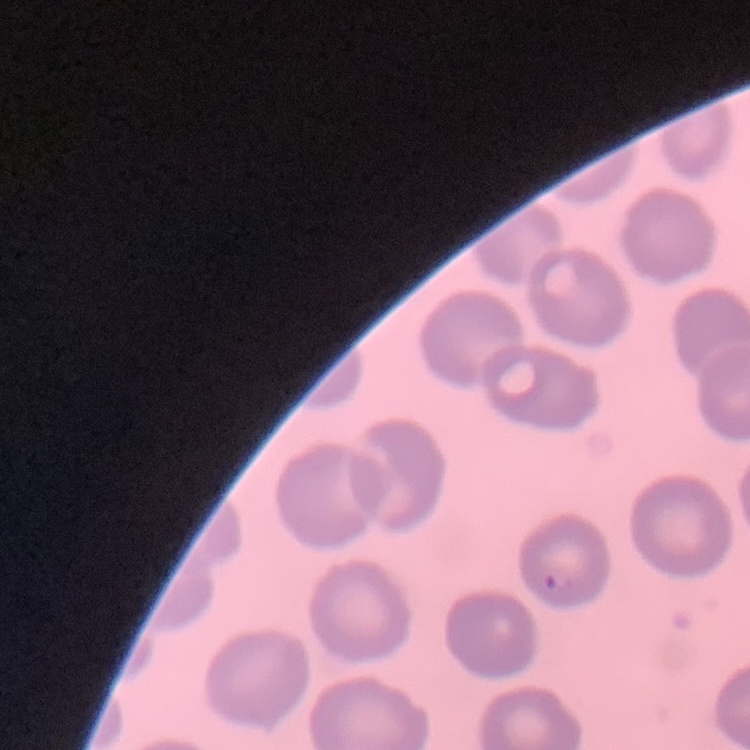
Summary:
  - Erythrocyte morphology: no rouleaux formation
  - Preparation: thin peripheral smear
  - Image type: square crop of a larger photomicrograph
  - Stain: Field's or Giemsa